Name the parasite shown.
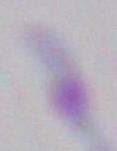
Toxoplasma gondii.

modality: micrograph
magnification: 1000x